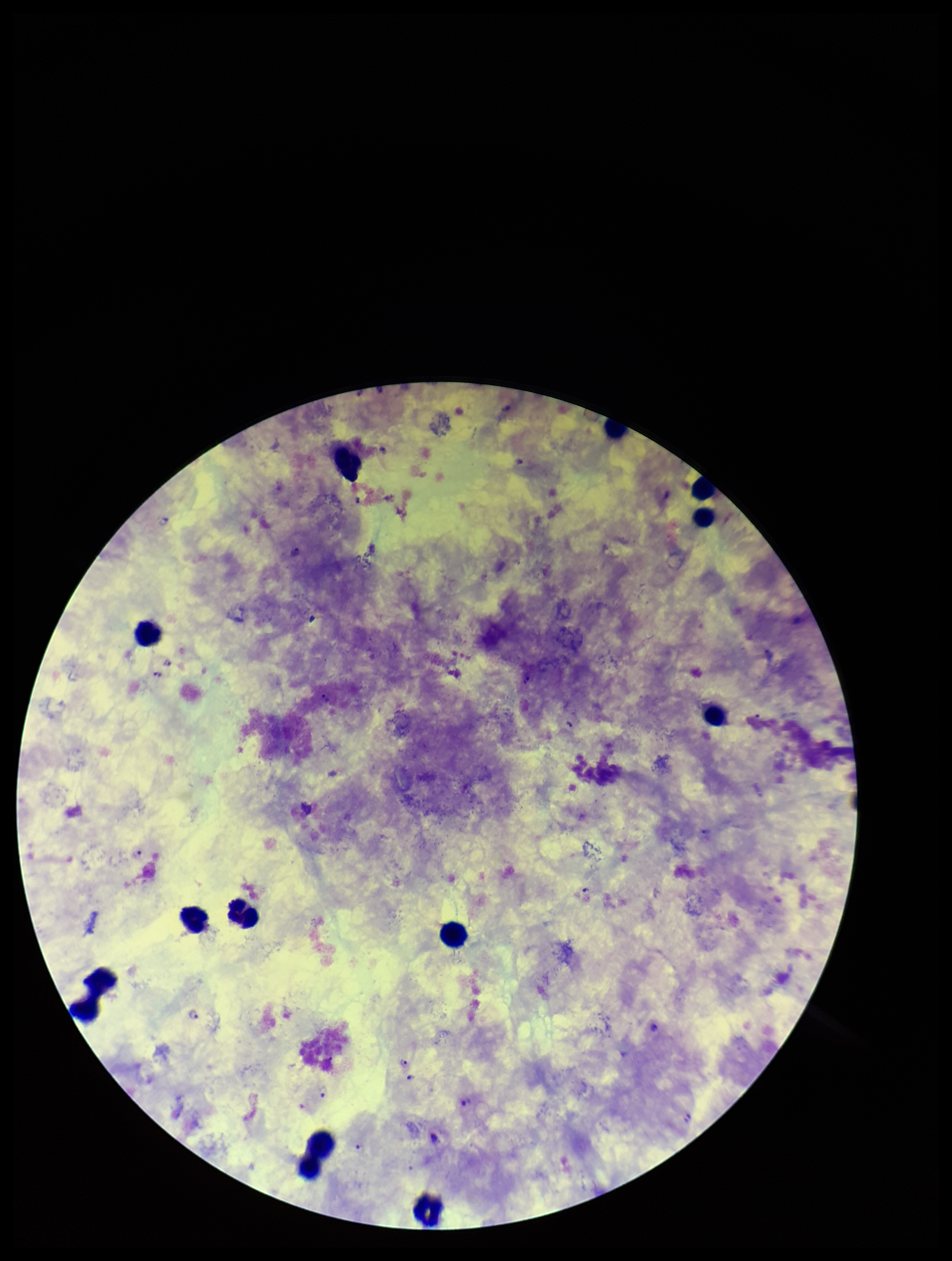
{
  "species_reported_for_this_patient": "Plasmodium falciparum",
  "image_size": "952×1261 pixels",
  "field_of_view": "one from this slide",
  "preparation": "thick",
  "patient_malaria_status": "infected",
  "leukocyte_count": 13,
  "plasmodium_parasites": "identified",
  "stain": "Giemsa",
  "parasite_count": 12,
  "capture": "smartphone photograph through the microscope eyepiece"
}